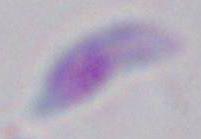

Summary:
  - Magnification: 1000x
  - Modality: micrograph
  - Identification: Toxoplasma gondii